Locate every blood parasite and identify its species.
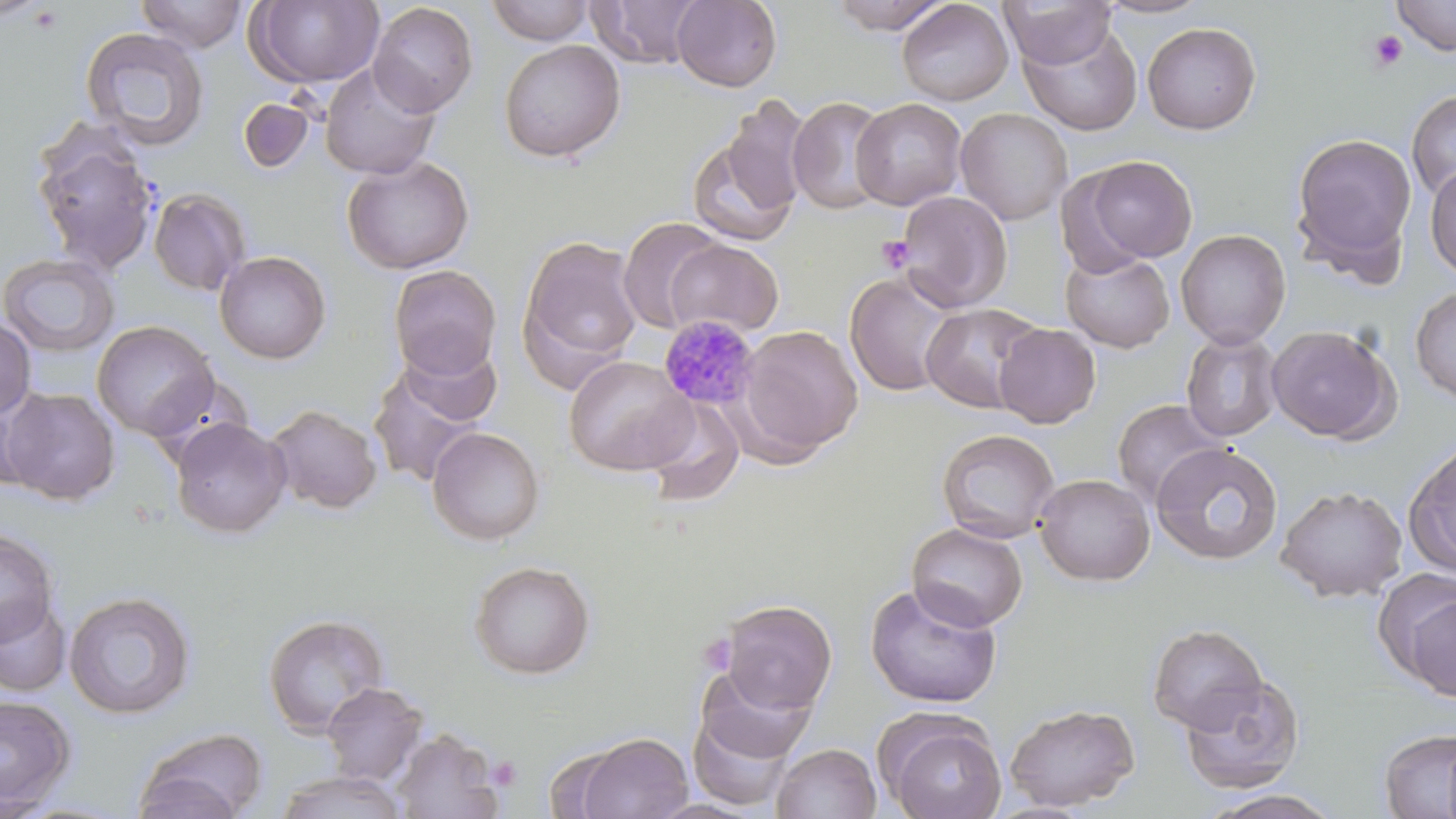
Approximate bounding boxes as named x1/y1/x2/y2 corners in pixels.
Plasmodium malariae-infected red blood cells: (x1=657, y1=314, x2=761, y2=411).
No Plasmodium falciparum, Plasmodium ovale, Plasmodium vivax, Babesia divergens, or Trypanosoma brucei observed.

Uninfected red blood cell locations: (x1=134, y1=0, x2=250, y2=53), (x1=671, y1=0, x2=782, y2=91), (x1=827, y1=0, x2=954, y2=34), (x1=896, y1=0, x2=1013, y2=106), (x1=999, y1=0, x2=1118, y2=70), (x1=1094, y1=0, x2=1213, y2=19), (x1=1392, y1=0, x2=1456, y2=56), (x1=245, y1=1, x2=385, y2=88), (x1=484, y1=1, x2=596, y2=45), (x1=586, y1=1, x2=705, y2=69), (x1=368, y1=2, x2=478, y2=117), (x1=1142, y1=21, x2=1262, y2=135), (x1=1019, y1=22, x2=1143, y2=137), (x1=79, y1=26, x2=211, y2=151), (x1=498, y1=39, x2=626, y2=163), (x1=320, y1=62, x2=441, y2=180), (x1=1406, y1=90, x2=1456, y2=203), (x1=719, y1=95, x2=813, y2=218), (x1=787, y1=96, x2=892, y2=215), (x1=237, y1=97, x2=314, y2=173), (x1=851, y1=97, x2=967, y2=210), (x1=955, y1=108, x2=1073, y2=225), (x1=31, y1=124, x2=160, y2=275), (x1=685, y1=132, x2=800, y2=246), (x1=1290, y1=133, x2=1418, y2=270), (x1=341, y1=155, x2=474, y2=274), (x1=1079, y1=155, x2=1198, y2=265), (x1=1425, y1=164, x2=1456, y2=281), (x1=148, y1=187, x2=252, y2=296), (x1=896, y1=191, x2=1013, y2=311), (x1=618, y1=217, x2=725, y2=334), (x1=1175, y1=229, x2=1291, y2=349), (x1=519, y1=235, x2=643, y2=381), (x1=666, y1=239, x2=784, y2=337), (x1=214, y1=250, x2=331, y2=364), (x1=1061, y1=251, x2=1175, y2=352), (x1=0, y1=252, x2=120, y2=358), (x1=388, y1=265, x2=502, y2=381), (x1=845, y1=271, x2=962, y2=396), (x1=1410, y1=287, x2=1456, y2=404), (x1=921, y1=302, x2=1045, y2=414), (x1=0, y1=318, x2=36, y2=420), (x1=91, y1=320, x2=219, y2=440), (x1=994, y1=323, x2=1101, y2=428), (x1=1266, y1=324, x2=1399, y2=444), (x1=738, y1=325, x2=863, y2=457), (x1=1180, y1=330, x2=1284, y2=442), (x1=398, y1=339, x2=502, y2=427), (x1=564, y1=355, x2=695, y2=476), (x1=366, y1=361, x2=489, y2=490), (x1=1, y1=387, x2=120, y2=504), (x1=0, y1=388, x2=42, y2=494), (x1=642, y1=395, x2=744, y2=505), (x1=1110, y1=398, x2=1229, y2=510), (x1=265, y1=404, x2=383, y2=514), (x1=170, y1=417, x2=291, y2=538), (x1=427, y1=426, x2=546, y2=545), (x1=936, y1=427, x2=1060, y2=543), (x1=1403, y1=438, x2=1456, y2=577), (x1=1150, y1=441, x2=1284, y2=566), (x1=1034, y1=473, x2=1155, y2=586), (x1=1275, y1=484, x2=1408, y2=602), (x1=906, y1=522, x2=1028, y2=632), (x1=0, y1=528, x2=59, y2=647), (x1=469, y1=560, x2=595, y2=679), (x1=865, y1=582, x2=1002, y2=708), (x1=63, y1=590, x2=196, y2=719), (x1=1403, y1=592, x2=1455, y2=704), (x1=0, y1=597, x2=71, y2=697), (x1=718, y1=598, x2=837, y2=713), (x1=262, y1=613, x2=391, y2=737), (x1=1147, y1=623, x2=1268, y2=733), (x1=693, y1=664, x2=817, y2=773), (x1=1178, y1=672, x2=1306, y2=794), (x1=321, y1=682, x2=429, y2=786), (x1=0, y1=695, x2=77, y2=813), (x1=1004, y1=703, x2=1140, y2=811), (x1=878, y1=711, x2=1008, y2=819), (x1=133, y1=726, x2=268, y2=819), (x1=1378, y1=726, x2=1456, y2=818), (x1=391, y1=728, x2=505, y2=819), (x1=568, y1=731, x2=694, y2=819), (x1=772, y1=743, x2=881, y2=819), (x1=272, y1=770, x2=411, y2=818), (x1=1201, y1=790, x2=1345, y2=818). Platelet locations: (x1=28, y1=5, x2=64, y2=35), (x1=1368, y1=29, x2=1407, y2=72), (x1=876, y1=235, x2=915, y2=274), (x1=698, y1=632, x2=739, y2=676), (x1=488, y1=756, x2=522, y2=790). Slide-level diagnosis: Plasmodium malariae. Light microscopy. Captured at 1000x magnification. May-Grünwald-Giemsa stain. Image is 1456×819 pixels. One field of a larger specimen. Thin blood smear.